Classify this cell by malaria status.
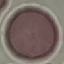

Uninfected.

image type = cell patch, automatically extracted from a larger field of view and resized to 64 × 64 pixels
capture = smartphone through the microscope eyepiece
preparation = thin smear
stain = Giemsa